Assess the morphology of the erythrocytes.
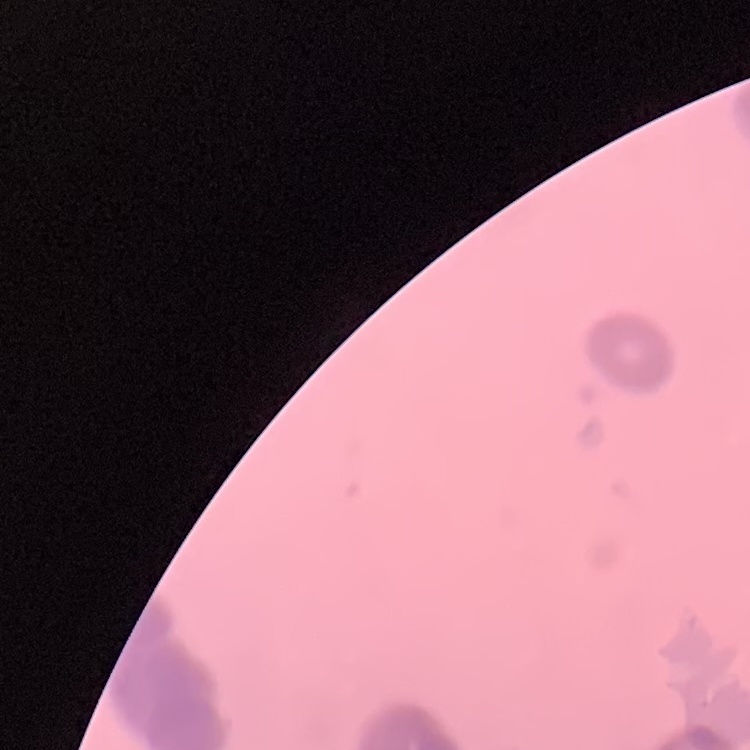
They show rouleaux formation.

Thin blood smear. One tile cut from a larger photomicrograph. Field's or Giemsa stain.